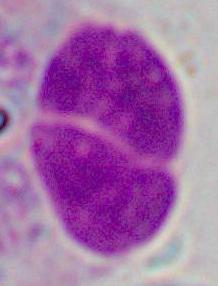

Summary:
  - Identification: leukocyte
  - Modality: photomicrograph
  - Magnification: 1000x